Assess this cell for malaria.
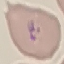
It is parasitized.

Giemsa-stained preparation. Thin blood film. Acquired by smartphone through the microscope eyepiece. Cell patch, automatically extracted from a larger field of view and resized to 64 × 64 pixels.